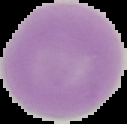 Segmented cell region on a black background. Malaria status: uninfected. From a thin blood smear. Image is 127×124 pixels.